Assess the morphology of the erythrocytes.
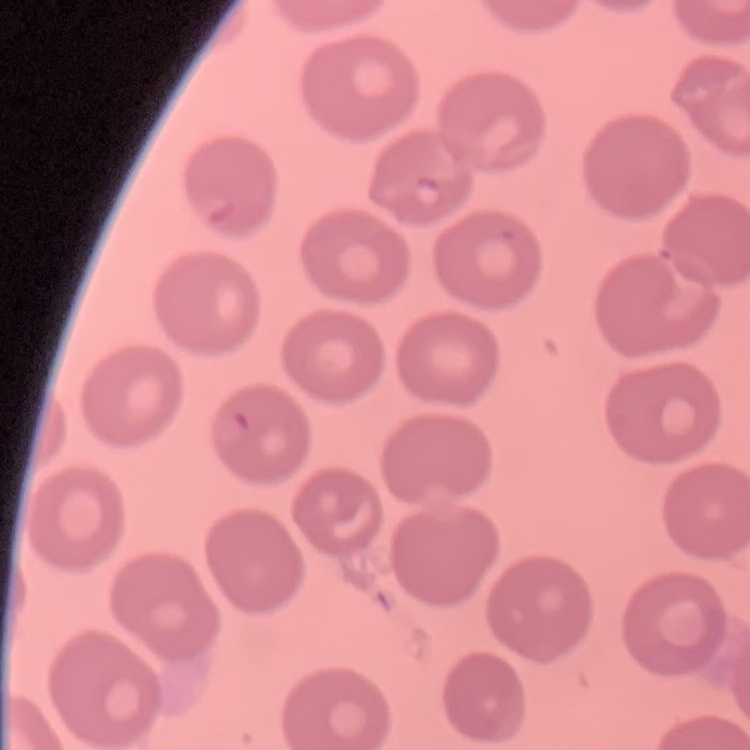
They show no rouleaux formation.

Summary:
  - Image type: one tile cut from a larger photomicrograph
  - Preparation: thin blood film
  - Stain: Field's or Giemsa